Comment on the morphology of the erythrocytes.
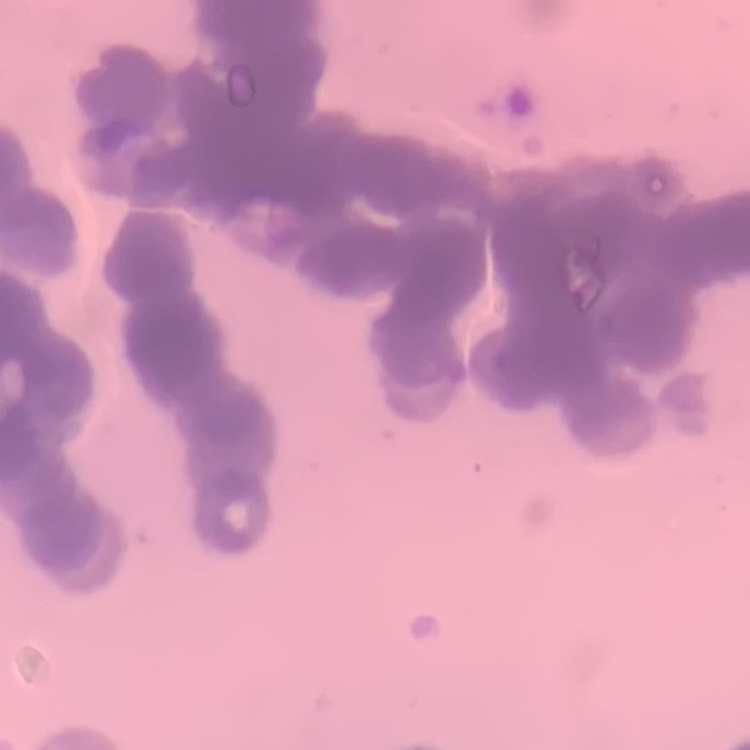

Rouleaux formation.

Summary:
  - Image type: one tile cut from a larger photomicrograph
  - Stain: Field's or Giemsa
  - Preparation: thin blood film